State which parasite is depicted.
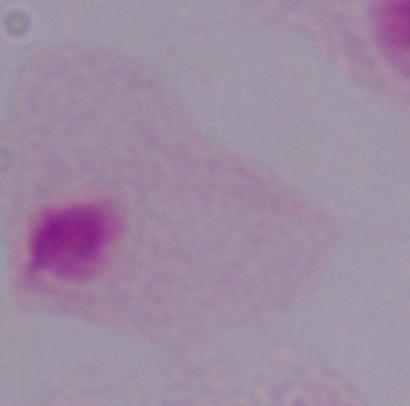

A trichomonad.

Photomicrograph. 1000x magnification.